Comment on the morphology of the red blood cells.
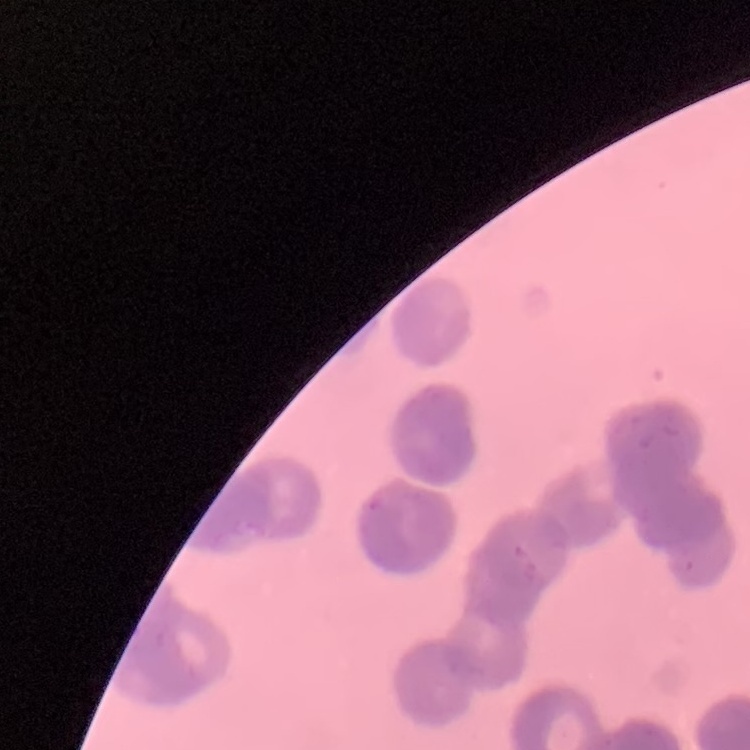
Rouleaux formation.

Summary:
  - Image type: square crop of a larger photomicrograph
  - Stain: Field's or Giemsa
  - Preparation: thin blood smear